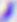

magnification = 400x
identification = Toxoplasma gondii
modality = micrograph